Locate every uninfected red blood cell.
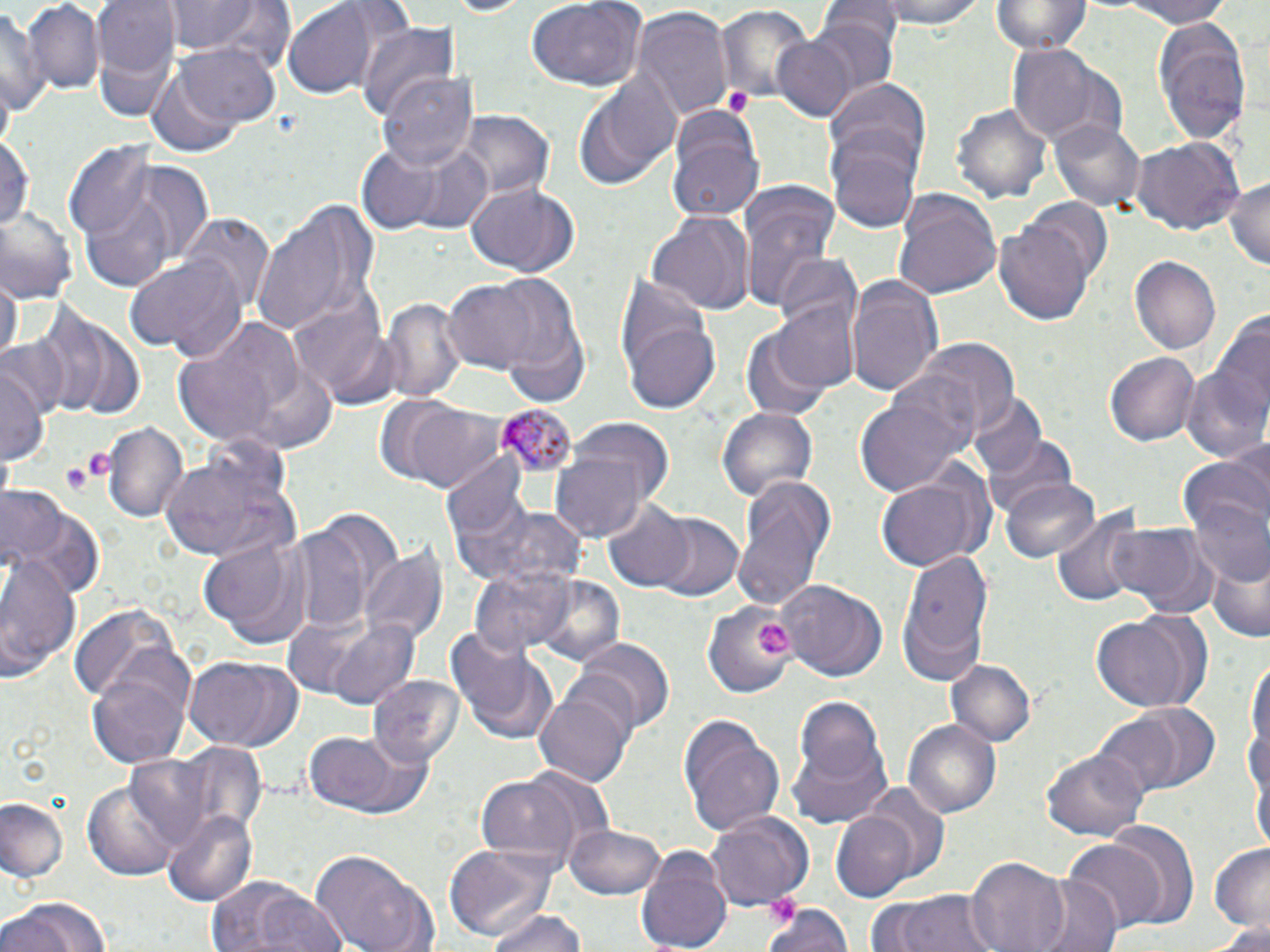

Approximate bounding boxes as named x1/y1/x2/y2 corners in pixels.
Uninfected red blood cells: (x1=93, y1=0, x2=181, y2=112), (x1=880, y1=0, x2=986, y2=31), (x1=992, y1=0, x2=1090, y2=58), (x1=1104, y1=0, x2=1241, y2=28), (x1=24, y1=1, x2=104, y2=95), (x1=161, y1=1, x2=278, y2=60), (x1=525, y1=1, x2=644, y2=91), (x1=821, y1=1, x2=900, y2=47), (x1=282, y1=2, x2=377, y2=98), (x1=0, y1=5, x2=42, y2=123), (x1=715, y1=5, x2=815, y2=108), (x1=632, y1=8, x2=733, y2=121), (x1=806, y1=15, x2=899, y2=101), (x1=1148, y1=15, x2=1252, y2=147), (x1=358, y1=23, x2=459, y2=122), (x1=772, y1=34, x2=859, y2=121), (x1=176, y1=41, x2=280, y2=129), (x1=1008, y1=45, x2=1123, y2=144), (x1=147, y1=66, x2=244, y2=156), (x1=379, y1=69, x2=480, y2=173), (x1=574, y1=69, x2=681, y2=192), (x1=828, y1=79, x2=933, y2=185), (x1=952, y1=99, x2=1050, y2=203), (x1=456, y1=109, x2=551, y2=202), (x1=668, y1=113, x2=765, y2=223), (x1=1051, y1=117, x2=1145, y2=212), (x1=0, y1=130, x2=34, y2=237), (x1=1130, y1=136, x2=1243, y2=234), (x1=353, y1=140, x2=468, y2=234), (x1=830, y1=140, x2=920, y2=232), (x1=65, y1=144, x2=208, y2=288), (x1=409, y1=148, x2=493, y2=233), (x1=1225, y1=173, x2=1270, y2=271), (x1=464, y1=182, x2=581, y2=277), (x1=736, y1=187, x2=840, y2=315), (x1=892, y1=189, x2=1001, y2=302), (x1=247, y1=194, x2=379, y2=339), (x1=1026, y1=198, x2=1114, y2=280), (x1=0, y1=210, x2=80, y2=302), (x1=650, y1=211, x2=753, y2=317), (x1=185, y1=216, x2=275, y2=315), (x1=994, y1=220, x2=1094, y2=325), (x1=125, y1=252, x2=248, y2=361), (x1=1131, y1=255, x2=1224, y2=356), (x1=773, y1=256, x2=863, y2=341), (x1=0, y1=275, x2=20, y2=367), (x1=844, y1=275, x2=945, y2=396), (x1=487, y1=276, x2=590, y2=399), (x1=443, y1=279, x2=542, y2=372), (x1=382, y1=297, x2=465, y2=404), (x1=770, y1=299, x2=863, y2=395), (x1=290, y1=301, x2=394, y2=404), (x1=42, y1=306, x2=146, y2=419), (x1=170, y1=316, x2=318, y2=452), (x1=1187, y1=317, x2=1269, y2=463), (x1=625, y1=319, x2=721, y2=414), (x1=738, y1=328, x2=837, y2=422), (x1=5, y1=332, x2=72, y2=428), (x1=917, y1=337, x2=1020, y2=434), (x1=1105, y1=350, x2=1198, y2=446), (x1=3, y1=364, x2=46, y2=471), (x1=853, y1=386, x2=973, y2=499), (x1=968, y1=394, x2=1047, y2=481), (x1=387, y1=397, x2=512, y2=493), (x1=715, y1=407, x2=817, y2=506), (x1=560, y1=415, x2=676, y2=514), (x1=103, y1=420, x2=187, y2=521), (x1=982, y1=433, x2=1080, y2=526), (x1=159, y1=439, x2=299, y2=564), (x1=549, y1=452, x2=649, y2=541), (x1=1181, y1=462, x2=1270, y2=582), (x1=871, y1=473, x2=986, y2=572), (x1=439, y1=477, x2=582, y2=597), (x1=733, y1=477, x2=836, y2=612), (x1=999, y1=478, x2=1101, y2=563), (x1=0, y1=488, x2=100, y2=599), (x1=603, y1=502, x2=697, y2=590), (x1=1050, y1=512, x2=1147, y2=604), (x1=649, y1=513, x2=744, y2=602), (x1=1104, y1=525, x2=1216, y2=616), (x1=289, y1=526, x2=372, y2=635), (x1=198, y1=530, x2=319, y2=650), (x1=0, y1=548, x2=84, y2=679), (x1=360, y1=549, x2=447, y2=646), (x1=896, y1=549, x2=997, y2=684), (x1=1204, y1=549, x2=1269, y2=647), (x1=468, y1=564, x2=577, y2=658), (x1=529, y1=575, x2=625, y2=670), (x1=780, y1=579, x2=885, y2=682), (x1=704, y1=601, x2=802, y2=693), (x1=69, y1=605, x2=177, y2=708), (x1=1090, y1=613, x2=1202, y2=714), (x1=322, y1=616, x2=424, y2=711), (x1=445, y1=627, x2=556, y2=743), (x1=570, y1=635, x2=675, y2=734), (x1=86, y1=652, x2=196, y2=766), (x1=183, y1=655, x2=303, y2=752), (x1=1247, y1=656, x2=1269, y2=792), (x1=946, y1=660, x2=1036, y2=748), (x1=369, y1=675, x2=464, y2=769), (x1=534, y1=689, x2=631, y2=788), (x1=793, y1=693, x2=889, y2=803), (x1=1095, y1=710, x2=1194, y2=797), (x1=678, y1=716, x2=784, y2=838), (x1=904, y1=718, x2=1002, y2=819), (x1=303, y1=732, x2=433, y2=821), (x1=168, y1=740, x2=271, y2=838), (x1=788, y1=741, x2=892, y2=828), (x1=1042, y1=747, x2=1151, y2=841), (x1=121, y1=753, x2=217, y2=853), (x1=476, y1=775, x2=583, y2=863), (x1=84, y1=779, x2=183, y2=880), (x1=0, y1=797, x2=66, y2=883), (x1=163, y1=808, x2=259, y2=905), (x1=707, y1=809, x2=815, y2=909), (x1=832, y1=812, x2=920, y2=899), (x1=1102, y1=822, x2=1198, y2=923), (x1=567, y1=825, x2=666, y2=899), (x1=1065, y1=839, x2=1167, y2=932), (x1=442, y1=841, x2=564, y2=943), (x1=1207, y1=843, x2=1270, y2=929), (x1=635, y1=846, x2=734, y2=952), (x1=310, y1=848, x2=434, y2=952), (x1=965, y1=857, x2=1071, y2=952), (x1=1027, y1=875, x2=1122, y2=952), (x1=205, y1=878, x2=345, y2=952), (x1=877, y1=888, x2=1002, y2=952), (x1=3, y1=894, x2=112, y2=951), (x1=764, y1=901, x2=854, y2=952), (x1=482, y1=910, x2=590, y2=952), (x1=1199, y1=920, x2=1270, y2=950).

Platelet locations: (x1=722, y1=84, x2=753, y2=114), (x1=65, y1=452, x2=115, y2=491), (x1=61, y1=463, x2=92, y2=492), (x1=754, y1=619, x2=793, y2=656). Plasmodium malariae-infected red blood cell locations: (x1=495, y1=404, x2=579, y2=476). Slide-level diagnosis: Plasmodium malariae. Image is 1270×952 pixels. May-Grünwald-Giemsa stain. Thin blood film. Light microscopy. Single field of view. Captured at 1000x magnification.